Classify this cell by malaria status.
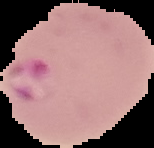
Parasitized.

{
  "preparation": "thin blood smear",
  "image_type": "cell region segmented out of the field of view; surrounding area masked to black",
  "image_size": "154×148 pixels"
}